State which cell type is depicted.
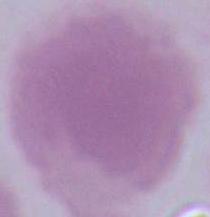

An erythrocyte.

Captured at 1000x magnification. Micrograph.